Describe the morphology of the red blood cells.
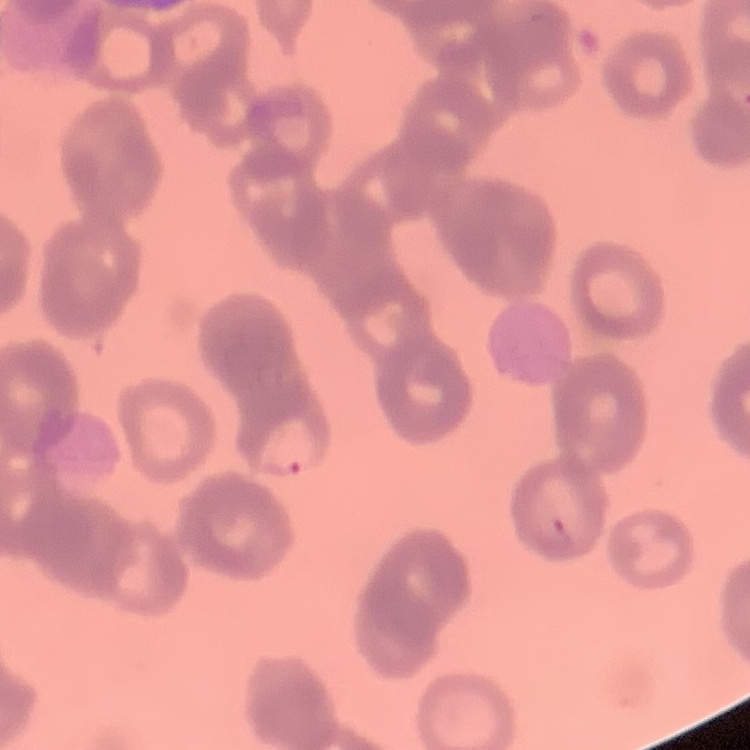

They show rouleaux formation.

stain = Field's or Giemsa
preparation = thin blood film
image type = square crop of a larger photomicrograph